Classify this cell by malaria status.
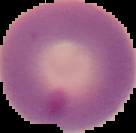

Parasitized.

From a thin blood smear. Segmented cell region on a black background. Image is 136×133 pixels.